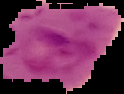

Summary:
  - Malaria status: parasitized
  - Image size: 124×94 pixels
  - Preparation: thin blood film
  - Image type: segmented cell region on a black background